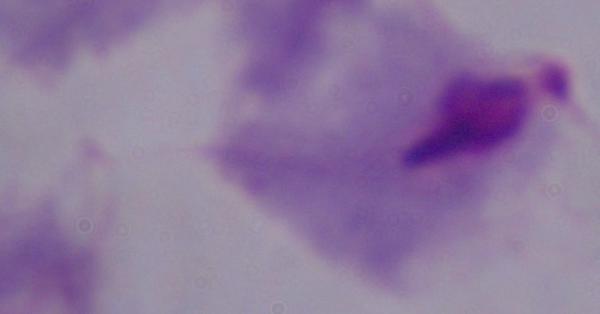

Micrograph. A trichomonad is seen. Captured at 1000x magnification.